Report the malaria status of this cell.
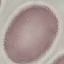

It is uninfected.

Summary:
  - Preparation: thin smear
  - Capture: smartphone camera at the microscope eyepiece
  - Stain: Giemsa
  - Image type: automatically extracted cell patch, resized to 64 × 64 pixels